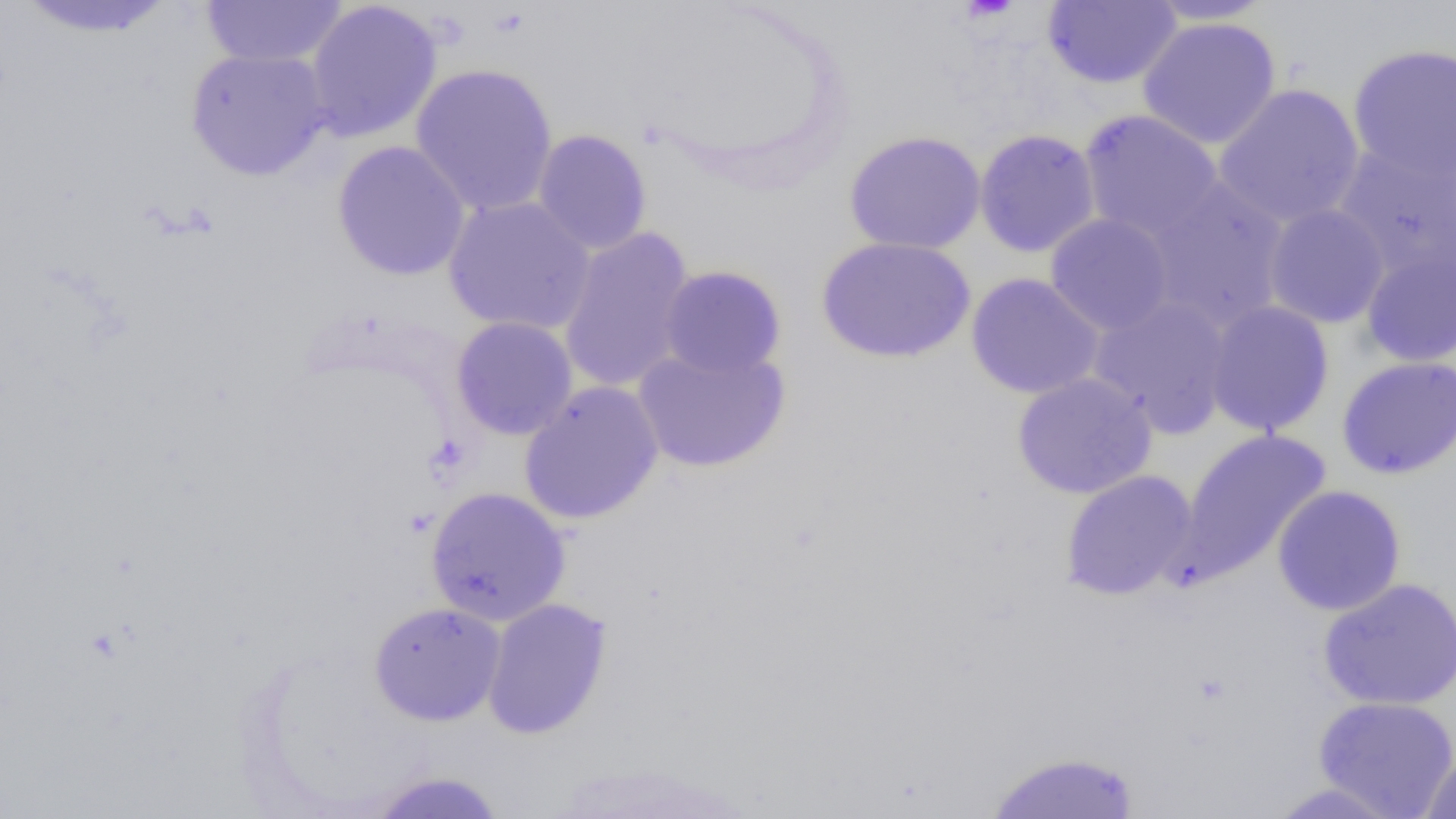
Summary:
  - Coordinate format: approximate bounding boxes as named x1/y1/x2/y2 corners in pixels
  - Uninfected red blood cell locations: (x1=13, y1=0, x2=178, y2=39), (x1=200, y1=1, x2=349, y2=68), (x1=304, y1=1, x2=443, y2=143), (x1=1042, y1=1, x2=1182, y2=89), (x1=1141, y1=1, x2=1280, y2=26), (x1=1138, y1=17, x2=1281, y2=149), (x1=1347, y1=43, x2=1456, y2=185), (x1=185, y1=48, x2=333, y2=181), (x1=410, y1=62, x2=559, y2=218), (x1=1213, y1=83, x2=1365, y2=230), (x1=1078, y1=109, x2=1224, y2=244), (x1=973, y1=128, x2=1101, y2=258), (x1=532, y1=129, x2=652, y2=255), (x1=843, y1=130, x2=987, y2=255), (x1=332, y1=140, x2=471, y2=282), (x1=1333, y1=144, x2=1455, y2=279), (x1=1143, y1=178, x2=1291, y2=332), (x1=443, y1=195, x2=596, y2=337), (x1=1263, y1=204, x2=1390, y2=328), (x1=1044, y1=213, x2=1175, y2=336), (x1=557, y1=227, x2=695, y2=394), (x1=815, y1=236, x2=977, y2=364), (x1=1360, y1=245, x2=1456, y2=367), (x1=658, y1=265, x2=787, y2=379), (x1=966, y1=272, x2=1105, y2=399), (x1=1088, y1=295, x2=1234, y2=438), (x1=1203, y1=301, x2=1335, y2=437), (x1=450, y1=316, x2=578, y2=441), (x1=632, y1=344, x2=791, y2=473), (x1=1336, y1=355, x2=1456, y2=480), (x1=1011, y1=372, x2=1157, y2=500), (x1=519, y1=381, x2=664, y2=525), (x1=1174, y1=427, x2=1333, y2=584), (x1=1059, y1=470, x2=1198, y2=601), (x1=1271, y1=485, x2=1407, y2=616), (x1=425, y1=486, x2=571, y2=626), (x1=1318, y1=578, x2=1456, y2=710), (x1=482, y1=597, x2=613, y2=739), (x1=369, y1=601, x2=506, y2=726), (x1=1312, y1=695, x2=1456, y2=818), (x1=984, y1=749, x2=1142, y2=818), (x1=1419, y1=749, x2=1456, y2=818), (x1=368, y1=770, x2=509, y2=818), (x1=1264, y1=781, x2=1407, y2=818)
  - Slide-level diagnosis: negative for blood parasites
  - Preparation: thin blood smear
  - Modality: light microscopy
  - Field of view: single
  - Image size: 1456×819 pixels
  - Magnification: 1000x